Report the malaria status of this cell.
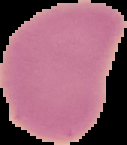
It is uninfected.

{
  "image_type": "segmented cell region on a black background",
  "preparation": "thin blood smear",
  "image_size": "127×145 pixels"
}